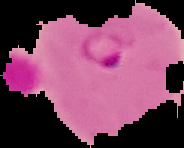
Summary:
  - Image size: 184×148 pixels
  - Preparation: thin blood film
  - Result: malaria parasites detected
  - Image type: segmented cell region with the area outside set to black